Assess this cell for malaria.
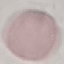

It is uninfected.

Summary:
  - Image type: cell patch, automatically extracted from a larger field of view and resized to 64 × 64 pixels
  - Capture: smartphone camera at the microscope eyepiece
  - Preparation: thin blood smear
  - Stain: Giemsa